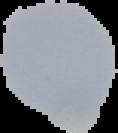
Summary:
  - Preparation: thin blood smear
  - Image size: 118×133 pixels
  - Malaria status: uninfected
  - Image type: segmented cell region with the area outside set to black